Give the extent of all Plasmodium vivax-infected red blood cells.
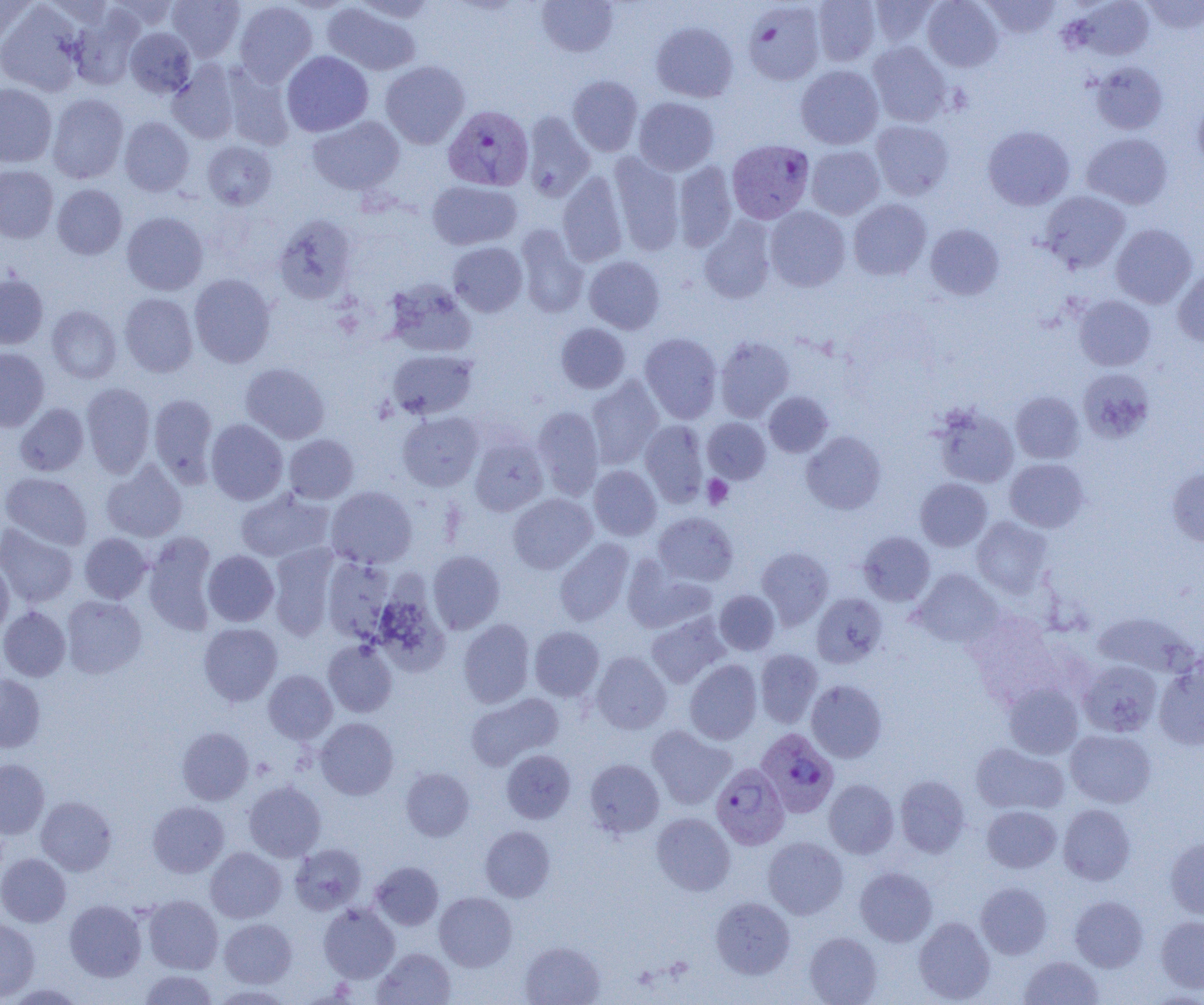

Approximate bounding boxes as [x1, y1, x2, y2] in pixels.
Plasmodium vivax-infected red blood cells: [443, 105, 534, 191], [728, 142, 816, 227], [759, 731, 842, 820], [716, 767, 794, 853].

{
  "slide_level_diagnosis": "Plasmodium vivax",
  "modality": "light microscopy",
  "image_size": "1204×1005 pixels",
  "preparation": "thin blood film",
  "magnification": "1000x",
  "uninfected_red_blood_cell_locations": "approximate bounding boxes as [x1, y1, x2, y2] in pixels: [0, 0, 37, 51], [107, 0, 179, 30], [167, 0, 245, 61], [354, 0, 437, 23], [536, 0, 619, 57], [812, 0, 880, 66], [868, 0, 940, 47], [922, 0, 1003, 72], [980, 0, 1060, 39], [1071, 0, 1155, 60], [1141, 0, 1204, 34], [234, 1, 317, 86], [0, 2, 85, 96], [323, 2, 421, 76], [743, 2, 825, 86], [68, 8, 143, 90], [651, 22, 738, 103], [125, 27, 196, 98], [867, 41, 952, 126], [281, 51, 373, 136], [168, 60, 240, 144], [380, 60, 470, 149], [1091, 62, 1168, 134], [222, 63, 295, 150], [796, 64, 884, 149], [567, 75, 643, 156], [0, 83, 57, 167], [47, 94, 128, 183], [633, 97, 719, 175], [1193, 97, 1204, 170], [521, 112, 595, 202], [308, 116, 405, 195], [119, 117, 194, 196], [870, 120, 954, 200], [983, 125, 1074, 210], [1082, 133, 1172, 209], [202, 141, 277, 210], [806, 145, 885, 219], [609, 153, 684, 255], [673, 161, 737, 251], [0, 165, 58, 243], [558, 172, 628, 266], [427, 180, 522, 250], [53, 184, 127, 259], [1039, 191, 1131, 273], [848, 198, 931, 280], [765, 206, 851, 291], [122, 211, 208, 295], [273, 215, 358, 304], [699, 216, 777, 304], [1110, 223, 1197, 309], [515, 224, 588, 318], [925, 224, 1004, 300], [448, 241, 527, 317], [584, 256, 665, 334], [1173, 267, 1204, 347], [0, 273, 48, 349], [189, 274, 276, 368], [385, 281, 476, 357], [119, 293, 198, 377], [1074, 295, 1155, 371], [47, 305, 122, 384], [555, 323, 630, 393], [640, 333, 722, 423], [715, 337, 794, 422], [0, 348, 49, 431], [387, 349, 477, 419], [240, 362, 330, 444], [1078, 369, 1154, 443], [586, 377, 663, 469], [81, 382, 155, 477], [764, 391, 832, 457], [1011, 391, 1084, 463], [149, 394, 218, 486], [15, 403, 89, 476], [931, 404, 1019, 488], [533, 406, 604, 500], [398, 412, 483, 491], [703, 418, 770, 483], [206, 419, 288, 505], [641, 420, 708, 507], [802, 431, 886, 514], [284, 434, 358, 503], [470, 435, 548, 516], [1005, 458, 1089, 532], [101, 461, 187, 542], [589, 465, 661, 541], [1167, 466, 1204, 547], [1, 472, 92, 549], [915, 478, 992, 550], [326, 486, 417, 568], [235, 488, 334, 563], [508, 494, 597, 573], [654, 512, 738, 586], [972, 516, 1053, 597], [0, 523, 78, 607], [859, 532, 935, 605], [79, 533, 151, 603], [143, 533, 218, 635], [554, 538, 634, 626], [269, 545, 340, 640], [757, 547, 833, 629], [203, 550, 279, 626], [428, 551, 505, 634], [323, 556, 396, 642], [0, 557, 13, 636], [623, 559, 715, 633], [913, 568, 1003, 647], [715, 589, 779, 655], [373, 591, 450, 676], [812, 593, 888, 668], [62, 595, 146, 678], [0, 606, 70, 681], [968, 611, 1062, 705], [1093, 611, 1195, 677], [646, 612, 729, 688], [458, 619, 534, 708], [199, 622, 282, 705], [529, 626, 604, 700], [323, 640, 397, 717], [755, 649, 823, 727], [591, 651, 672, 734], [1077, 659, 1163, 737], [684, 660, 762, 744], [1154, 661, 1204, 750], [263, 669, 337, 744], [0, 673, 45, 752], [806, 680, 887, 762], [1002, 682, 1084, 758], [466, 693, 563, 770], [315, 718, 398, 799], [646, 726, 735, 809], [177, 727, 254, 805], [1065, 729, 1156, 807], [971, 743, 1068, 815], [501, 750, 575, 823], [0, 759, 49, 839], [585, 759, 664, 837], [401, 768, 474, 841], [894, 774, 970, 857], [824, 779, 899, 858], [244, 781, 326, 861], [36, 796, 116, 875], [148, 801, 229, 877], [1058, 804, 1135, 885], [981, 805, 1061, 873], [651, 812, 735, 895], [480, 826, 555, 902], [763, 836, 848, 919], [1165, 837, 1204, 919], [290, 844, 366, 915], [206, 847, 286, 922], [0, 853, 71, 927], [370, 862, 444, 930], [855, 867, 937, 946], [976, 882, 1052, 959], [434, 892, 516, 971], [1070, 895, 1148, 971], [144, 896, 223, 974], [711, 897, 795, 979], [65, 900, 146, 981], [319, 903, 399, 983], [1156, 916, 1204, 993], [914, 917, 995, 1003], [0, 918, 40, 1001], [219, 919, 296, 987], [805, 931, 882, 1004], [520, 941, 605, 1005], [374, 948, 456, 1005], [1019, 955, 1103, 1004], [139, 970, 218, 1004], [4, 983, 87, 1004], [210, 984, 293, 1004]",
  "platelet_locations": "approximate bounding boxes as [x1, y1, x2, y2] in pixels: [702, 475, 733, 509]",
  "field_of_view": "one of a larger specimen"
}